Rate the background quality.
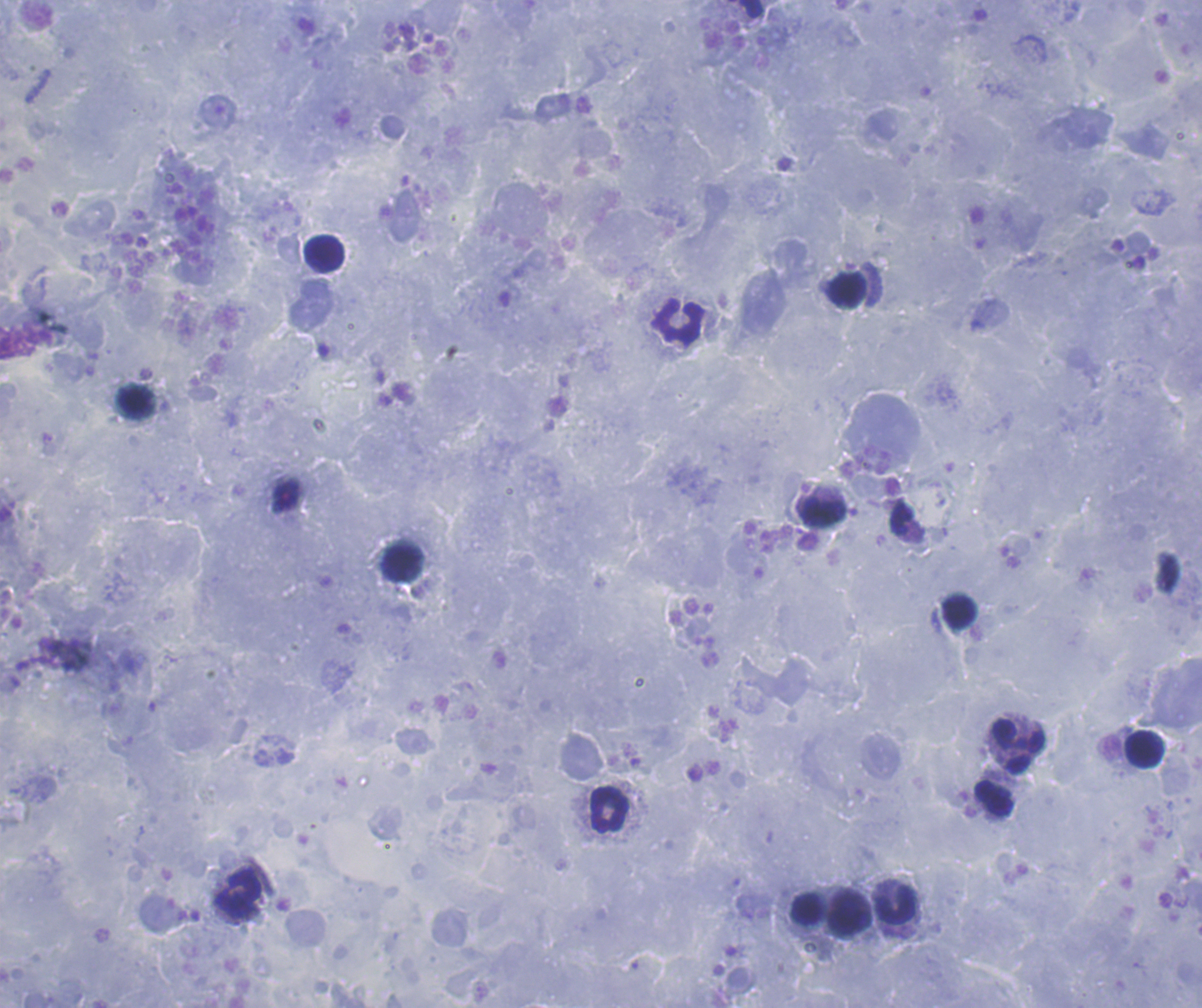
Satisfactory.

Approximate centers as (x, y) in pixels.
Summary:
  - Leukocyte locations: (323, 253), (848, 290), (680, 321), (134, 402), (823, 512), (401, 561), (960, 613), (1017, 746), (1145, 749), (993, 798), (609, 808), (239, 893), (896, 906), (808, 908), (849, 912)
  - Stain: Romanowsky
  - Image size: 1202×1008 pixels
  - Result: negative for Plasmodium parasites
  - Preparation: thick blood film
  - Context: previously used in an actual diagnosis
  - Coloration quality: good
  - Field of view: single
  - Magnification: 100x